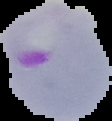
image_type: segmented cell region with the area outside set to black
image_size: 112×121 pixels
result: Plasmodium parasites detected
preparation: thin blood smear